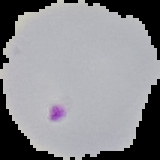
{
  "image_type": "segmented cell region on a black background",
  "image_size": "160×160 pixels",
  "malaria_status": "parasitized",
  "preparation": "thin blood film"
}